Identify the parasite.
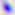
Toxoplasma gondii.

Photomicrograph. 400x magnification.